Look for Plasmodium parasites.
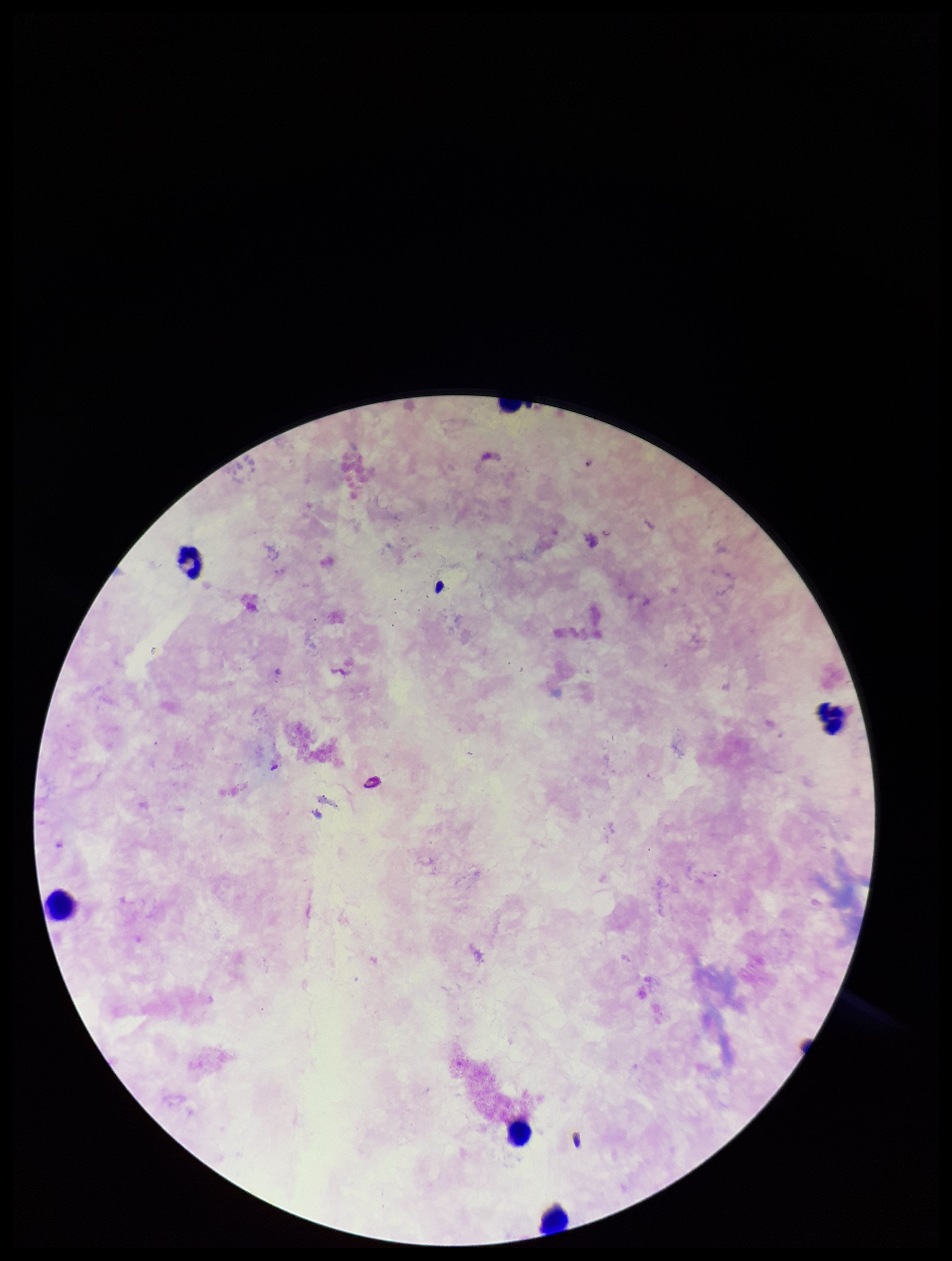

None seen.

Parasite count: 0. Patient malaria status: negative. One field from this slide. Leukocyte count: 5. Image is 952×1261 pixels. Smartphone photograph taken through the eyepiece of a microscope. Giemsa stain. Preparation: thick.